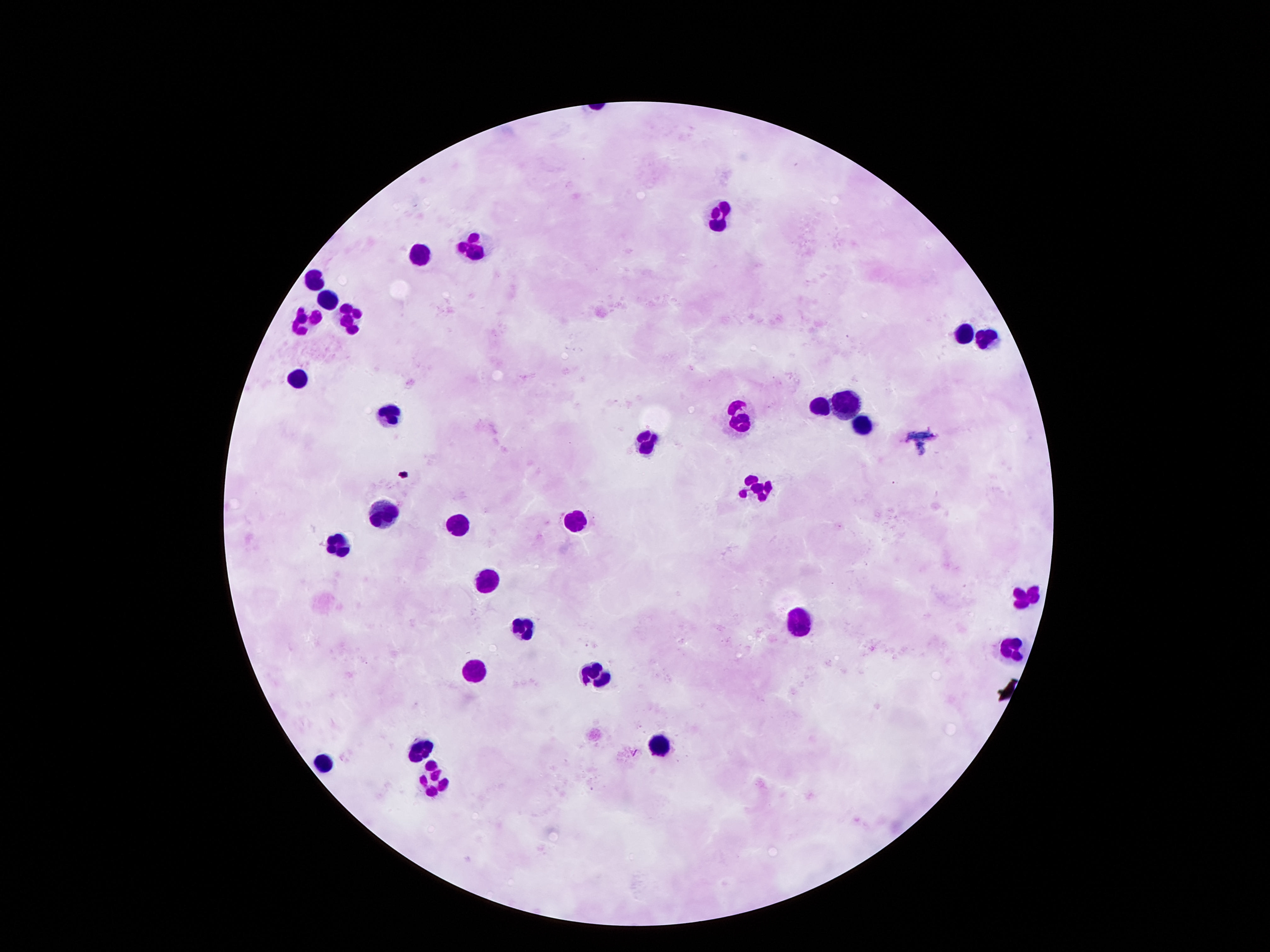
Approximate object centers, in pixels from the top-left corner. Leukocyte locations: (x=718, y=215), (x=476, y=245), (x=417, y=256), (x=315, y=274), (x=327, y=300), (x=353, y=310), (x=304, y=320), (x=962, y=329), (x=987, y=334), (x=296, y=377), (x=847, y=399), (x=825, y=401), (x=387, y=414), (x=739, y=414), (x=860, y=426), (x=642, y=437), (x=756, y=488), (x=385, y=514), (x=574, y=522), (x=459, y=526), (x=340, y=546), (x=485, y=574), (x=1030, y=594), (x=800, y=617), (x=521, y=622), (x=1012, y=647), (x=473, y=667), (x=593, y=668), (x=660, y=739), (x=420, y=744), (x=322, y=759), (x=430, y=781). Patient malaria status: uninfected. Image is 1270×952 pixels. Giemsa stain. Thick peripheral-blood smear. 100x magnification. Smartphone photograph taken through the microscope eyepiece. Single field of view.